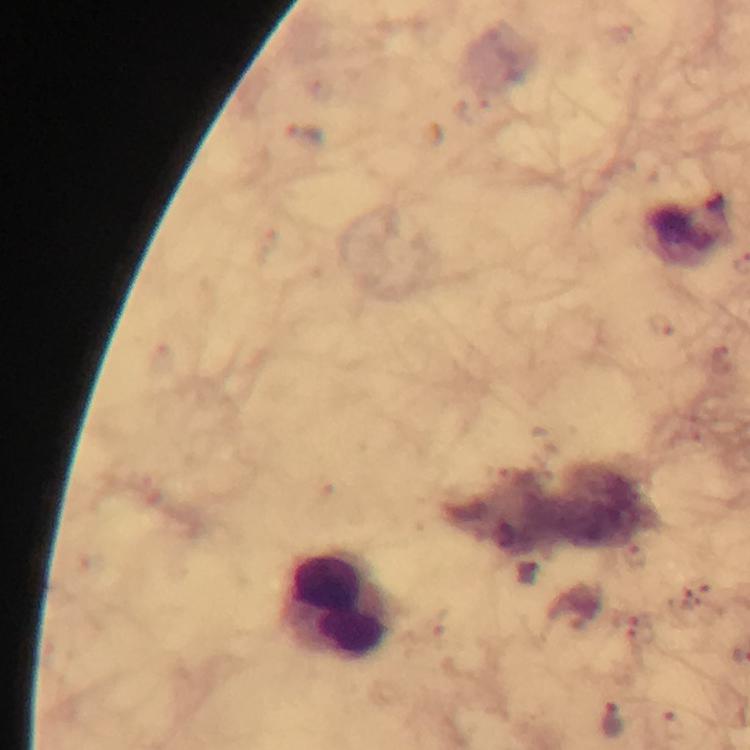
Approximate centers as {x, y} in pixels.
Summary:
  - Malaria parasite locations: {305, 135}, {527, 572}, {613, 720}
  - Leukocyte locations: {336, 606}
  - Capture: smartphone photograph through a microscope
  - Context: from a diagnostic examination for malaria
  - Preparation: thick blood smear
  - Immersion oil: used
  - Cropped from: one field of view
  - Stain: Giemsa
  - Magnification: 100x
  - Image size: 750×750 pixels